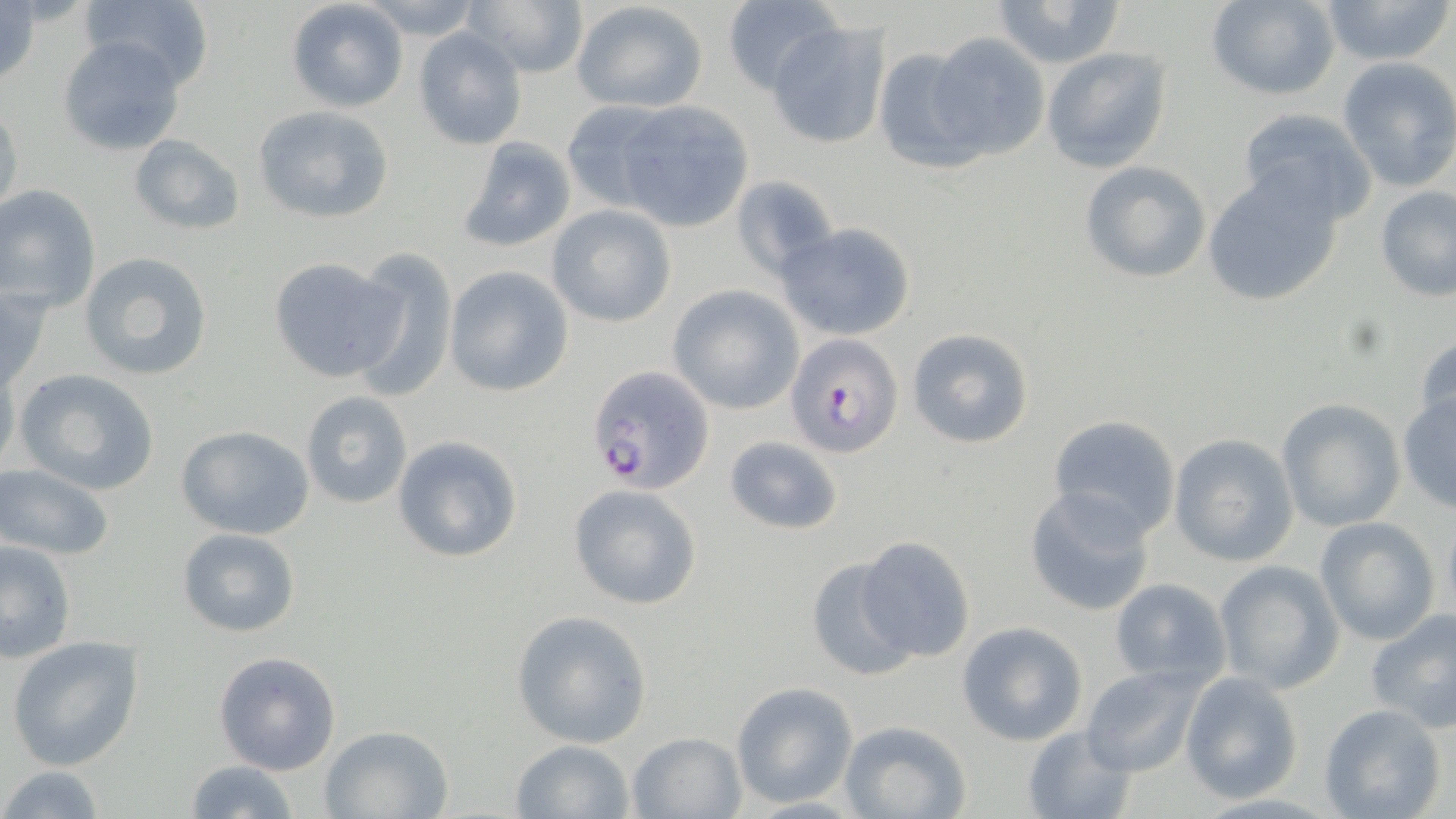 Approximate bounding boxes as [x1, y1, x2, y2] in pixels. Plasmodium falciparum-infected red blood cell locations: [787, 334, 904, 456], [586, 365, 714, 492]. Uninfected red blood cell locations: [78, 0, 215, 85], [286, 0, 409, 113], [355, 0, 486, 38], [464, 0, 587, 80], [987, 0, 1129, 69], [1206, 0, 1339, 99], [1314, 0, 1456, 66], [572, 1, 709, 113], [720, 1, 841, 95], [0, 2, 41, 91], [767, 20, 889, 149], [413, 29, 527, 150], [928, 32, 1050, 160], [57, 36, 186, 157], [1042, 46, 1173, 173], [871, 48, 985, 174], [1336, 56, 1456, 192], [556, 98, 679, 215], [0, 101, 23, 219], [614, 102, 753, 232], [252, 105, 395, 224], [1236, 107, 1377, 224], [128, 133, 245, 234], [455, 136, 577, 253], [1079, 159, 1214, 282], [1202, 168, 1345, 307], [731, 176, 839, 281], [0, 185, 101, 309], [1375, 185, 1456, 302], [546, 205, 677, 327], [777, 222, 916, 342], [348, 246, 458, 402], [79, 252, 214, 381], [266, 256, 402, 382], [442, 265, 574, 396], [0, 283, 53, 396], [668, 286, 803, 413], [906, 327, 1034, 451], [1412, 334, 1456, 437], [0, 358, 20, 479], [13, 368, 160, 495], [300, 391, 414, 509], [1397, 391, 1456, 512], [1274, 399, 1405, 533], [1046, 415, 1182, 540], [174, 424, 316, 540], [1168, 434, 1299, 566], [393, 435, 522, 564], [723, 435, 843, 534], [0, 464, 115, 560], [569, 483, 705, 609], [1023, 486, 1157, 617], [1441, 512, 1456, 629], [1314, 518, 1440, 646], [177, 527, 302, 637], [856, 533, 977, 663], [1, 540, 76, 662], [804, 556, 916, 683], [1214, 561, 1344, 695], [1108, 578, 1232, 688], [1365, 609, 1456, 733], [511, 611, 653, 748], [957, 621, 1088, 746], [6, 637, 144, 771], [213, 650, 343, 775], [1082, 665, 1206, 776], [1178, 671, 1304, 802], [730, 683, 856, 807], [1318, 703, 1448, 819], [836, 719, 974, 819], [1021, 724, 1139, 819], [319, 725, 453, 818], [626, 731, 747, 818], [509, 738, 636, 818], [182, 759, 298, 819], [1, 764, 108, 819]. Slide-level diagnosis: Plasmodium falciparum. 1000x magnification. May-Grünwald-Giemsa-stained preparation. Thin blood film. Single field of view. Optical microscopy. Image is 1456×819 pixels.